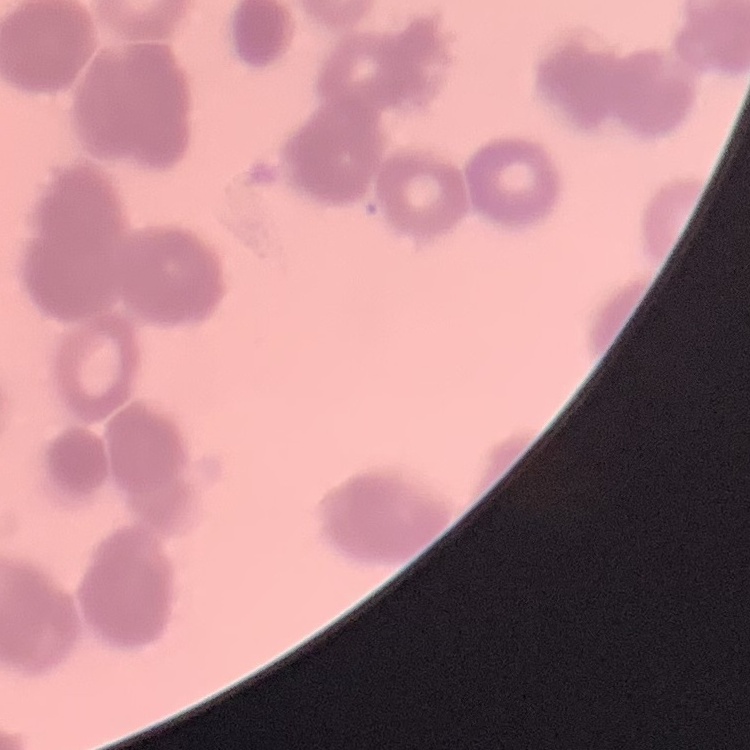
red blood cell morphology = rouleaux formation
image type = square crop of a larger photomicrograph
stain = Field's or Giemsa
preparation = thin blood film